Outline each blood parasite and name the species.
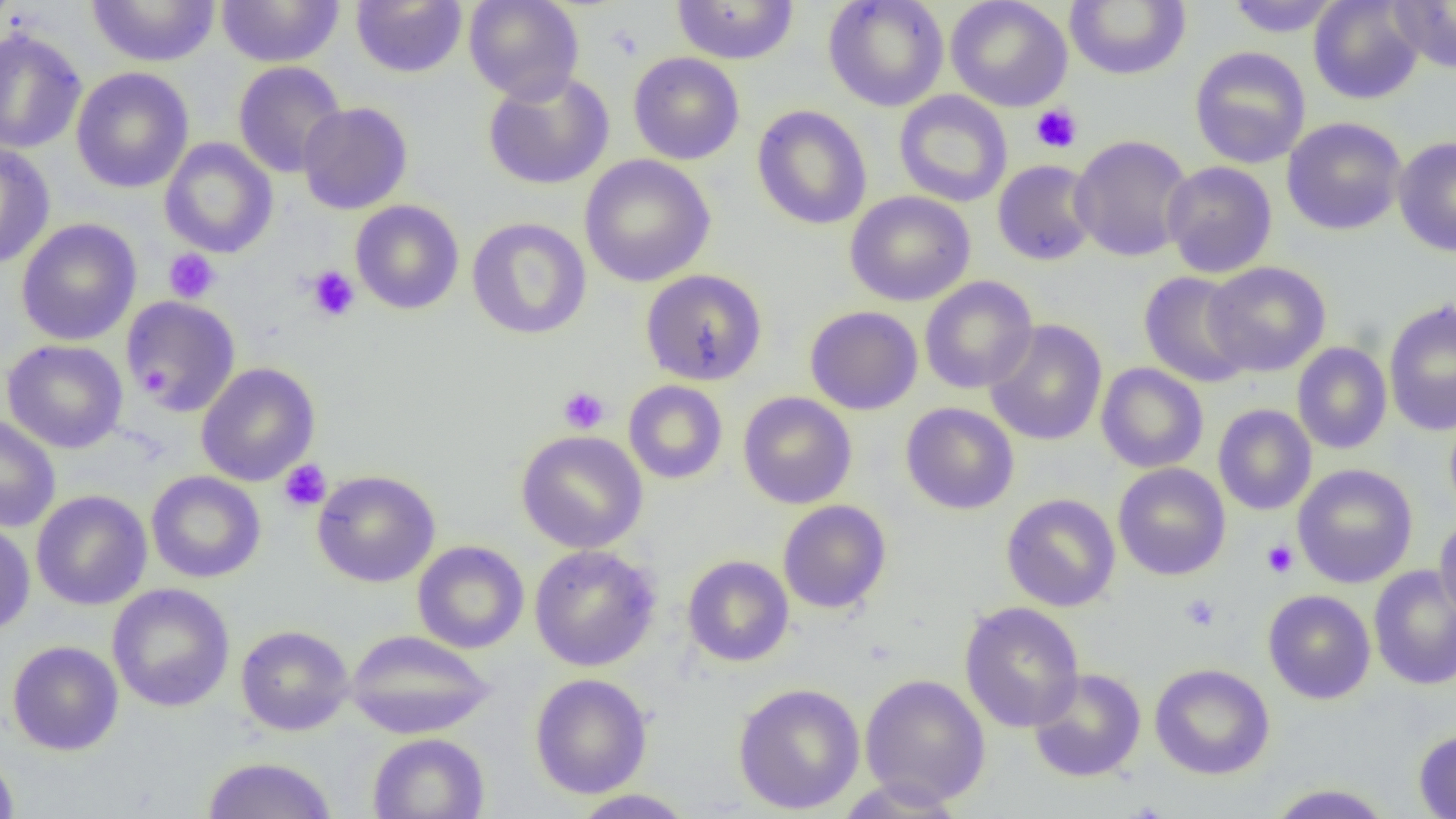

No blood parasites seen.

{
  "slide_level_diagnosis": "no evidence of blood parasites",
  "modality": "light microscopy",
  "magnification": "1000x",
  "field_of_view": "single",
  "platelet_locations": "approximate bounding boxes as named x1/y1/x2/y2 corners in pixels: (x1=1030, y1=104, x2=1083, y2=154), (x1=163, y1=249, x2=221, y2=303), (x1=306, y1=266, x2=360, y2=321), (x1=139, y1=364, x2=173, y2=395), (x1=558, y1=386, x2=610, y2=434), (x1=279, y1=459, x2=331, y2=512), (x1=1261, y1=539, x2=1299, y2=578), (x1=1181, y1=594, x2=1220, y2=631)",
  "image_size": "1456×819 pixels",
  "uninfected_red_blood_cell_locations": "approximate bounding boxes as named x1/y1/x2/y2 corners in pixels: (x1=85, y1=0, x2=220, y2=67), (x1=215, y1=0, x2=345, y2=67), (x1=463, y1=0, x2=584, y2=103), (x1=671, y1=0, x2=799, y2=65), (x1=823, y1=0, x2=949, y2=112), (x1=945, y1=0, x2=1073, y2=112), (x1=1064, y1=0, x2=1191, y2=81), (x1=1225, y1=0, x2=1343, y2=37), (x1=1309, y1=0, x2=1425, y2=105), (x1=351, y1=1, x2=468, y2=78), (x1=1388, y1=1, x2=1456, y2=73), (x1=0, y1=28, x2=87, y2=155), (x1=1189, y1=46, x2=1311, y2=169), (x1=628, y1=51, x2=745, y2=165), (x1=233, y1=61, x2=347, y2=178), (x1=71, y1=66, x2=194, y2=193), (x1=483, y1=70, x2=615, y2=190), (x1=894, y1=90, x2=1013, y2=208), (x1=297, y1=102, x2=413, y2=215), (x1=752, y1=105, x2=872, y2=230), (x1=1282, y1=117, x2=1407, y2=235), (x1=1070, y1=134, x2=1194, y2=262), (x1=1393, y1=136, x2=1456, y2=257), (x1=159, y1=138, x2=278, y2=258), (x1=0, y1=142, x2=55, y2=269), (x1=579, y1=154, x2=716, y2=287), (x1=992, y1=160, x2=1099, y2=266), (x1=1162, y1=160, x2=1277, y2=278), (x1=845, y1=191, x2=975, y2=306), (x1=350, y1=200, x2=464, y2=315), (x1=467, y1=217, x2=592, y2=340), (x1=16, y1=218, x2=142, y2=346), (x1=1203, y1=261, x2=1331, y2=377), (x1=641, y1=269, x2=768, y2=386), (x1=1139, y1=271, x2=1254, y2=388), (x1=919, y1=276, x2=1038, y2=394), (x1=122, y1=296, x2=242, y2=417), (x1=1384, y1=299, x2=1456, y2=437), (x1=805, y1=305, x2=922, y2=415), (x1=985, y1=319, x2=1107, y2=446), (x1=2, y1=339, x2=128, y2=454), (x1=1292, y1=342, x2=1392, y2=454), (x1=196, y1=362, x2=320, y2=486), (x1=1096, y1=363, x2=1209, y2=473), (x1=623, y1=380, x2=728, y2=484), (x1=738, y1=392, x2=856, y2=509), (x1=900, y1=402, x2=1019, y2=515), (x1=1213, y1=404, x2=1317, y2=516), (x1=1444, y1=407, x2=1456, y2=521), (x1=0, y1=414, x2=61, y2=533), (x1=516, y1=430, x2=648, y2=554), (x1=1113, y1=463, x2=1230, y2=581), (x1=1293, y1=464, x2=1418, y2=588), (x1=312, y1=469, x2=440, y2=587), (x1=146, y1=471, x2=266, y2=583), (x1=31, y1=490, x2=152, y2=610), (x1=1001, y1=493, x2=1120, y2=612), (x1=778, y1=500, x2=891, y2=614), (x1=1434, y1=515, x2=1456, y2=621), (x1=0, y1=518, x2=35, y2=635), (x1=412, y1=540, x2=529, y2=653), (x1=528, y1=544, x2=660, y2=671), (x1=683, y1=555, x2=794, y2=667), (x1=1368, y1=565, x2=1456, y2=690), (x1=107, y1=583, x2=235, y2=712), (x1=1263, y1=590, x2=1376, y2=703), (x1=959, y1=601, x2=1085, y2=733), (x1=236, y1=624, x2=354, y2=736), (x1=345, y1=629, x2=496, y2=739), (x1=7, y1=640, x2=124, y2=756), (x1=1150, y1=663, x2=1275, y2=780), (x1=1028, y1=668, x2=1146, y2=783), (x1=530, y1=673, x2=652, y2=799), (x1=860, y1=673, x2=991, y2=807), (x1=733, y1=682, x2=865, y2=814), (x1=1413, y1=728, x2=1456, y2=818), (x1=367, y1=732, x2=489, y2=819), (x1=0, y1=747, x2=20, y2=818), (x1=202, y1=756, x2=338, y2=819), (x1=832, y1=778, x2=969, y2=818), (x1=1264, y1=783, x2=1394, y2=818), (x1=568, y1=789, x2=697, y2=818)",
  "preparation": "thin blood film"
}